Locate and identify every blood parasite.
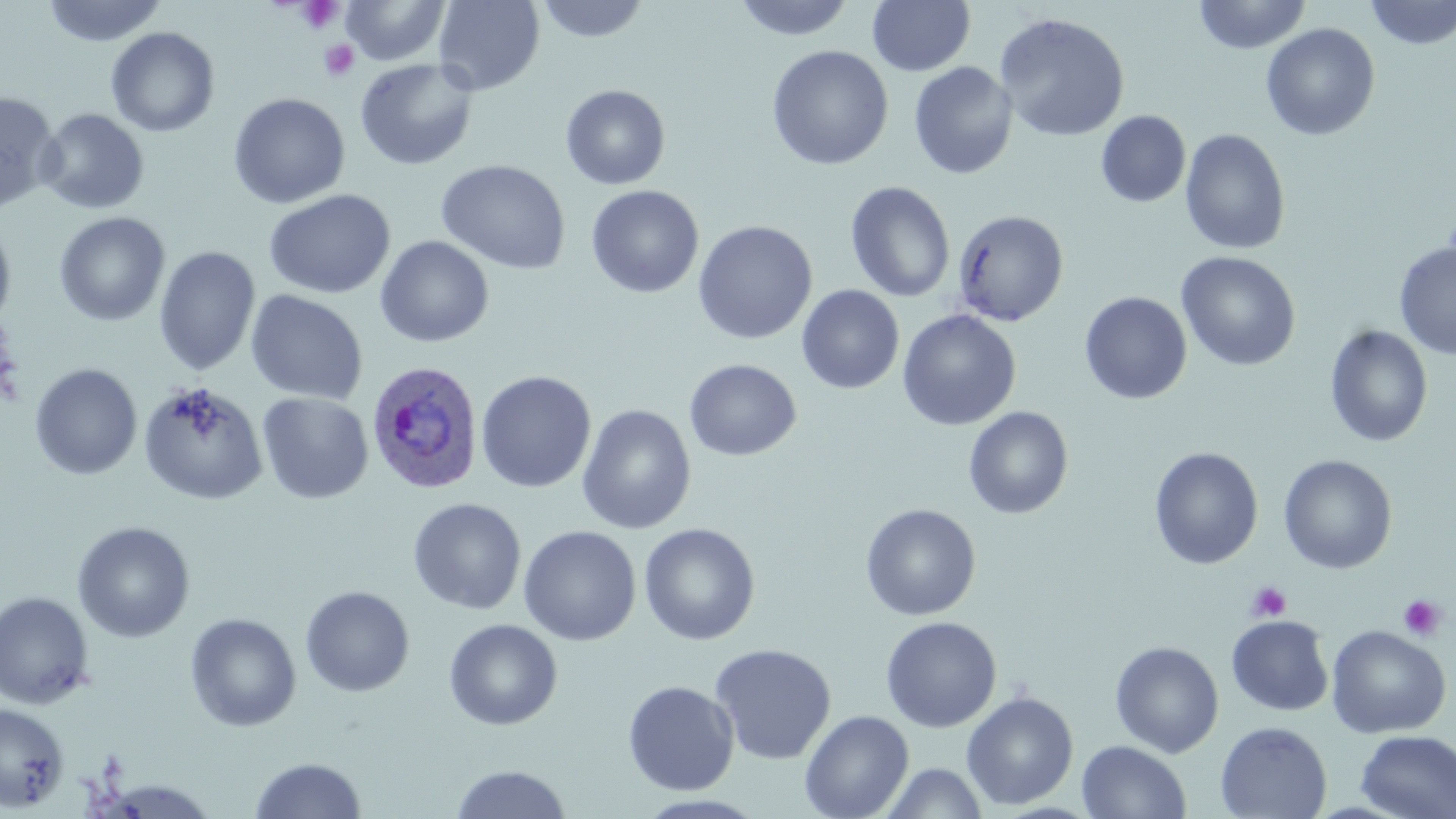

Approximate bounding boxes as named x1/y1/x2/y2 corners in pixels.
Plasmodium ovale-infected red blood cells: (x1=366, y1=359, x2=484, y2=494).
No Plasmodium falciparum, Plasmodium malariae, Plasmodium vivax, Babesia divergens, or Trypanosoma brucei observed.

{
  "slide_level_diagnosis": "Plasmodium ovale",
  "stain": "May-Grünwald-Giemsa",
  "platelet_locations": "approximate bounding boxes as named x1/y1/x2/y2 corners in pixels: (x1=295, y1=1, x2=344, y2=33), (x1=319, y1=39, x2=360, y2=82), (x1=1246, y1=581, x2=1291, y2=622), (x1=1397, y1=594, x2=1446, y2=641)",
  "field_of_view": "single",
  "magnification": "1000x",
  "preparation": "thin blood smear",
  "modality": "light microscopy",
  "image_size": "1456×819 pixels",
  "uninfected_red_blood_cell_locations": "approximate bounding boxes as named x1/y1/x2/y2 corners in pixels: (x1=339, y1=0, x2=451, y2=66), (x1=433, y1=0, x2=545, y2=95), (x1=535, y1=0, x2=652, y2=44), (x1=733, y1=0, x2=856, y2=41), (x1=867, y1=0, x2=976, y2=77), (x1=1193, y1=0, x2=1312, y2=54), (x1=41, y1=1, x2=167, y2=46), (x1=1365, y1=1, x2=1456, y2=50), (x1=994, y1=12, x2=1130, y2=143), (x1=1261, y1=23, x2=1380, y2=141), (x1=105, y1=27, x2=220, y2=137), (x1=766, y1=45, x2=894, y2=171), (x1=354, y1=58, x2=479, y2=171), (x1=908, y1=62, x2=1018, y2=179), (x1=560, y1=84, x2=671, y2=190), (x1=0, y1=92, x2=61, y2=213), (x1=228, y1=92, x2=350, y2=209), (x1=36, y1=108, x2=150, y2=214), (x1=1096, y1=110, x2=1191, y2=208), (x1=1180, y1=128, x2=1291, y2=256), (x1=436, y1=159, x2=571, y2=275), (x1=845, y1=181, x2=956, y2=303), (x1=586, y1=185, x2=704, y2=298), (x1=264, y1=189, x2=396, y2=299), (x1=952, y1=209, x2=1069, y2=326), (x1=54, y1=212, x2=170, y2=327), (x1=0, y1=220, x2=17, y2=329), (x1=693, y1=221, x2=817, y2=345), (x1=375, y1=235, x2=494, y2=348), (x1=1394, y1=241, x2=1456, y2=360), (x1=154, y1=246, x2=261, y2=377), (x1=1176, y1=251, x2=1301, y2=372), (x1=796, y1=285, x2=905, y2=394), (x1=246, y1=289, x2=368, y2=405), (x1=1079, y1=291, x2=1193, y2=405), (x1=897, y1=309, x2=1021, y2=431), (x1=1324, y1=325, x2=1433, y2=447), (x1=684, y1=359, x2=801, y2=461), (x1=29, y1=363, x2=143, y2=480), (x1=475, y1=370, x2=596, y2=493), (x1=138, y1=381, x2=268, y2=506), (x1=257, y1=392, x2=374, y2=504), (x1=576, y1=405, x2=696, y2=534), (x1=963, y1=407, x2=1074, y2=519), (x1=1149, y1=447, x2=1264, y2=569), (x1=1278, y1=454, x2=1398, y2=574), (x1=407, y1=497, x2=527, y2=615), (x1=860, y1=503, x2=981, y2=621), (x1=72, y1=521, x2=196, y2=643), (x1=638, y1=523, x2=760, y2=645), (x1=519, y1=525, x2=641, y2=645), (x1=300, y1=586, x2=415, y2=697), (x1=0, y1=591, x2=95, y2=709), (x1=185, y1=613, x2=302, y2=732), (x1=1226, y1=615, x2=1334, y2=716), (x1=880, y1=616, x2=1002, y2=733), (x1=443, y1=619, x2=563, y2=730), (x1=1326, y1=625, x2=1451, y2=738), (x1=1109, y1=640, x2=1225, y2=757), (x1=709, y1=643, x2=837, y2=764), (x1=623, y1=680, x2=739, y2=796), (x1=961, y1=691, x2=1079, y2=810), (x1=0, y1=703, x2=69, y2=811), (x1=799, y1=709, x2=914, y2=819), (x1=1215, y1=721, x2=1333, y2=819), (x1=1355, y1=731, x2=1456, y2=818), (x1=1076, y1=740, x2=1191, y2=819), (x1=249, y1=756, x2=367, y2=818), (x1=880, y1=762, x2=989, y2=819), (x1=450, y1=764, x2=572, y2=818), (x1=96, y1=779, x2=221, y2=817)"
}